Identify the parasite.
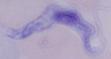

This is a trypanosome.

Summary:
  - Modality: micrograph
  - Magnification: 1000x